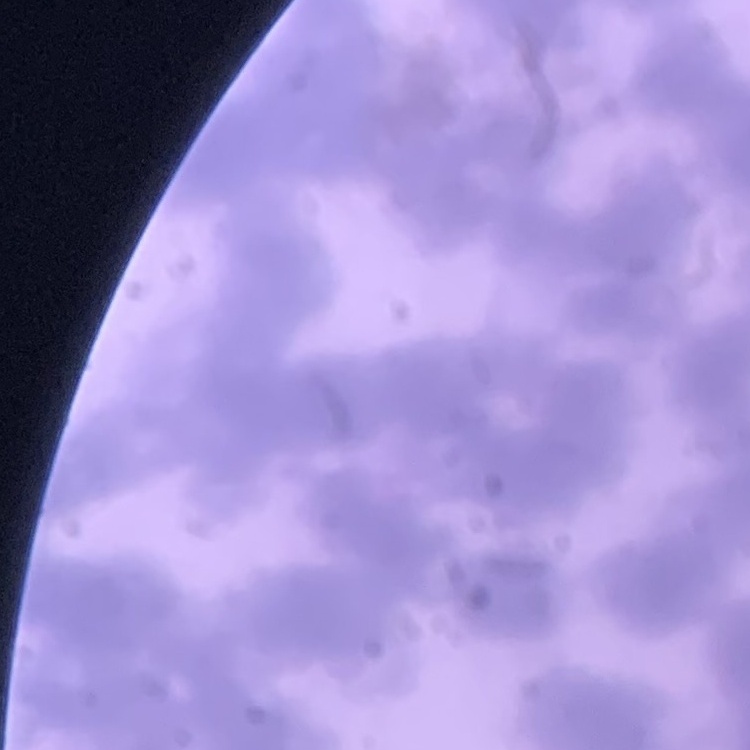
red blood cell morphology = rouleaux formation
image type = square crop of a larger photomicrograph
preparation = thin blood film
stain = Field's or Giemsa